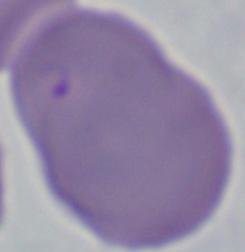
modality = photomicrograph
identification = Babesia
magnification = 1000x